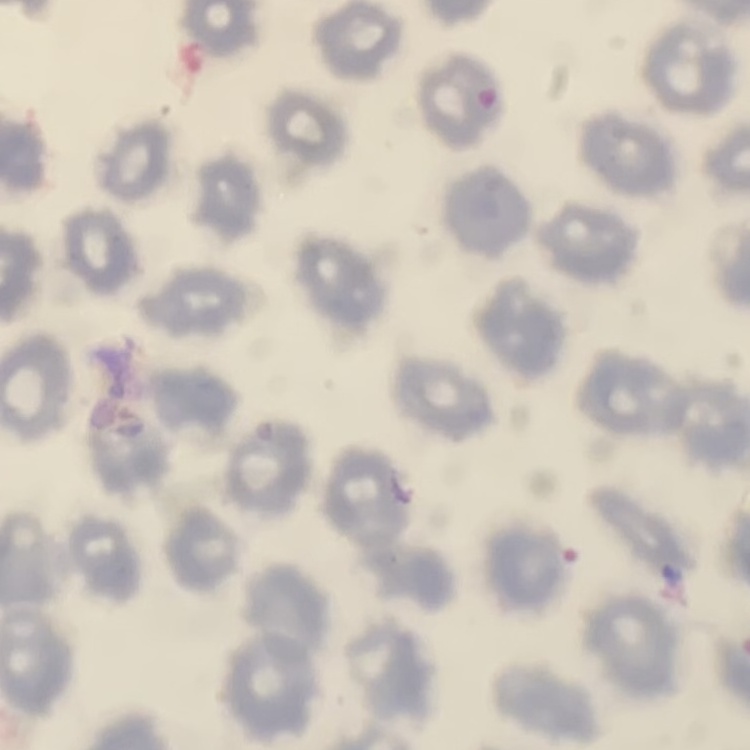
{
  "red_blood_cell_morphology": "no rouleaux formation",
  "image_type": "square crop of a larger photomicrograph",
  "preparation": "thin peripheral smear",
  "stain": "Field's or Giemsa"
}